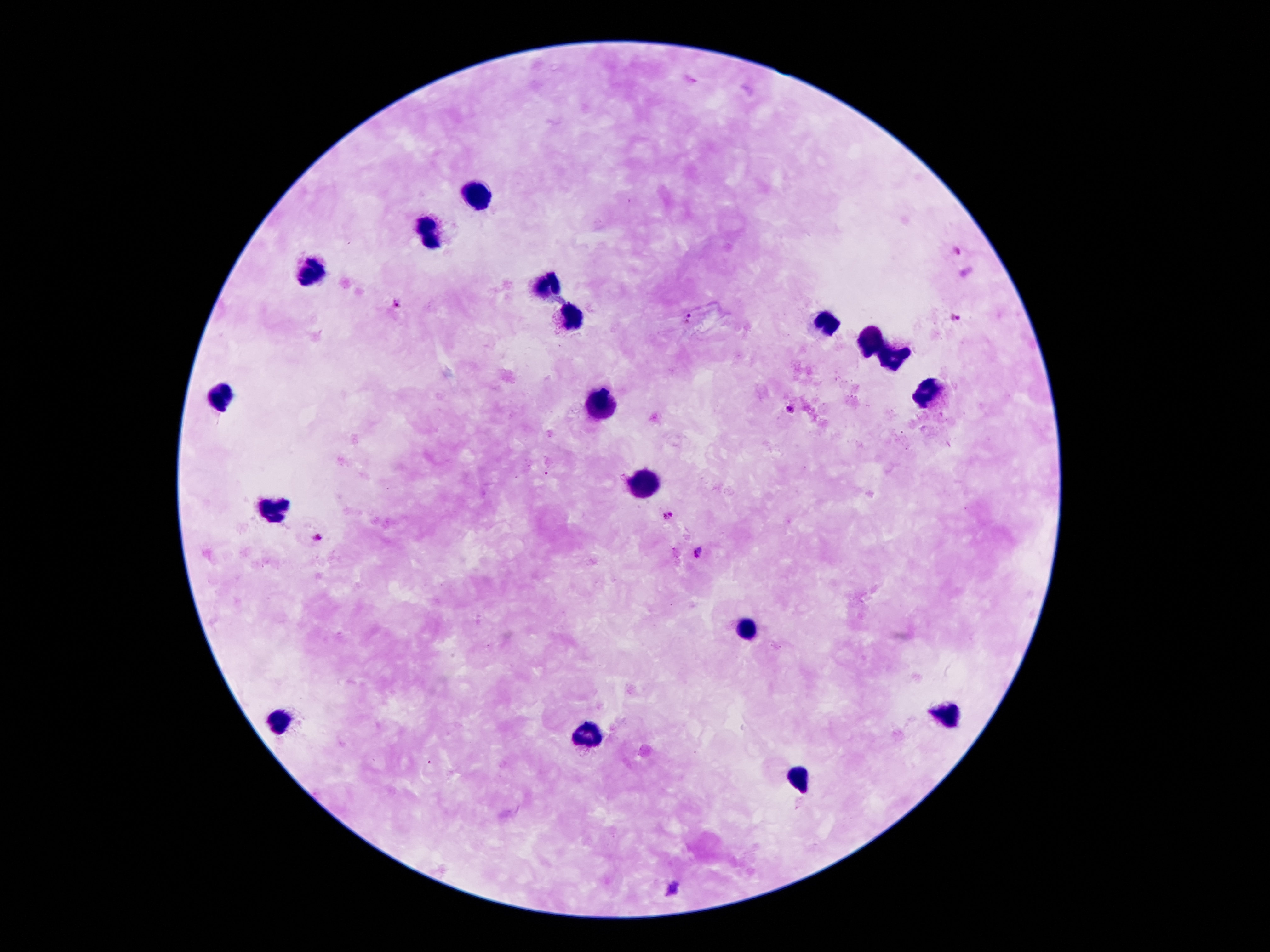

Approximate object centers, in pixels from the top-left corner.
Summary:
  - Leukocyte locations: (x=476, y=195), (x=431, y=231), (x=315, y=267), (x=547, y=287), (x=571, y=314), (x=827, y=319), (x=870, y=339), (x=890, y=360), (x=929, y=390), (x=222, y=394), (x=601, y=401), (x=646, y=479), (x=274, y=506), (x=748, y=629), (x=950, y=714), (x=278, y=720), (x=590, y=734), (x=801, y=776)
  - Malaria parasite locations: (x=959, y=250), (x=395, y=304), (x=954, y=315), (x=690, y=318), (x=791, y=410), (x=667, y=513), (x=317, y=536), (x=698, y=551), (x=675, y=889)
  - Image size: 1270×952 pixels
  - Field of view: single
  - Preparation: thick blood smear
  - Patient malaria status: infected with Plasmodium falciparum
  - Magnification: 100x
  - Capture: smartphone camera through the microscope eyepiece
  - Stain: Giemsa